Classify this cell by malaria status.
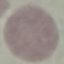
Uninfected.

{
  "preparation": "thin blood film",
  "capture": "smartphone through the microscope eyepiece",
  "image_type": "automatically extracted cell patch, resized to 64 × 64 pixels",
  "stain": "Giemsa"
}